Give the position of every malaria parasite and every leukocyte.
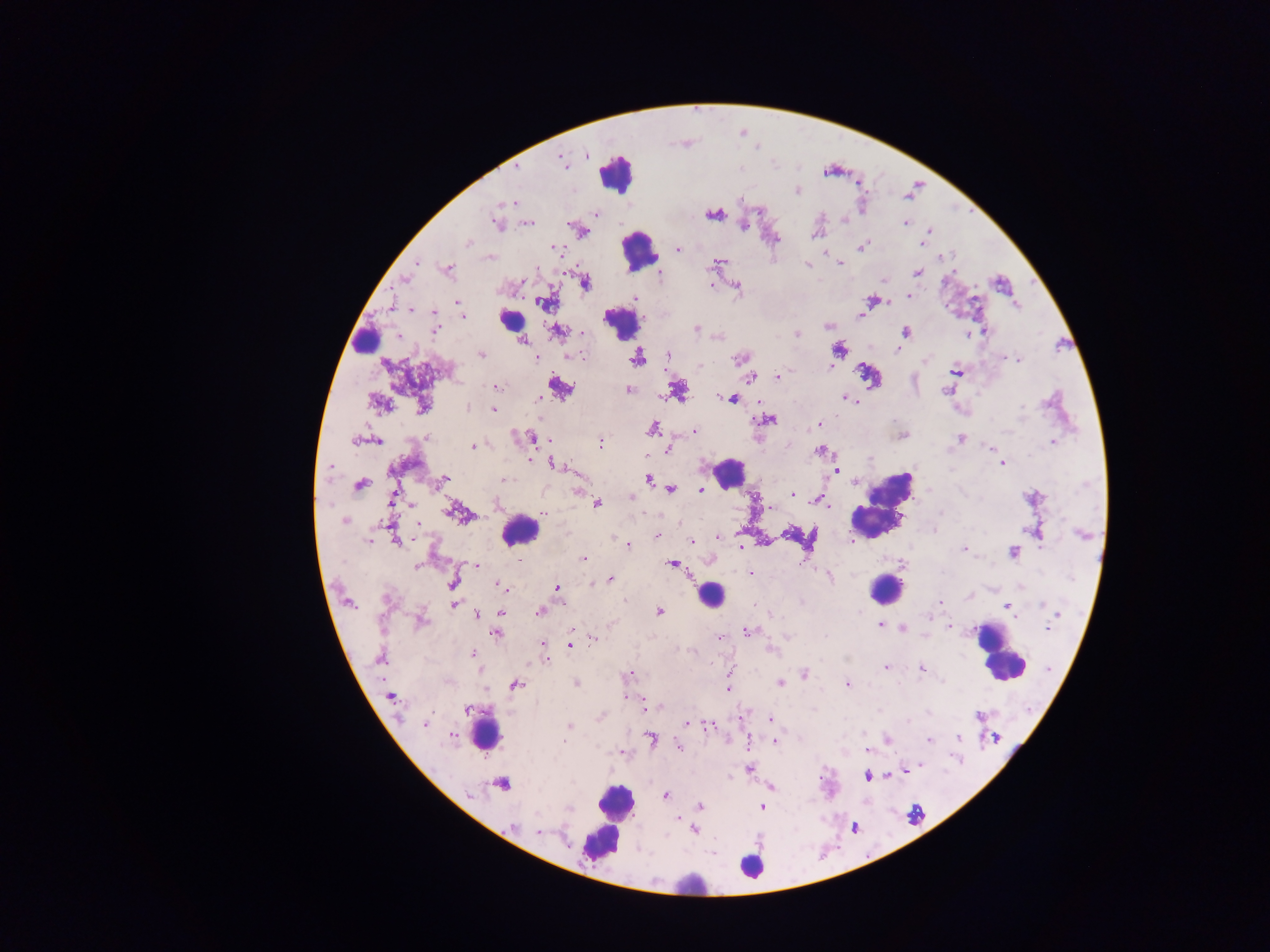
Approximate centers as x y in pixels.
Malaria parasites: 586 154; 561 160; 517 168; 797 190; 508 202; 758 209; 595 213; 713 214; 844 218; 905 222; 496 223; 526 223; 744 225; 582 232; 816 232; 926 236; 468 242; 922 242; 862 246; 555 249; 678 249; 824 251; 490 257; 720 261; 840 263; 416 264; 807 265; 447 270; 917 272; 660 275; 404 280; 584 282; 885 282; 735 284; 710 285; 908 295; 634 298; 871 300; 458 303; 546 303; 1015 304; 409 310; 460 311; 433 313; 861 313; 462 315; 828 327; 694 328; 435 329; 557 330; 906 331; 984 331; 583 332; 796 334; 966 334; 521 338; 898 347; 838 351; 668 354; 480 355; 582 357; 740 357; 636 358; 1003 358; 536 359; 1019 359; 829 366; 956 370; 777 376; 749 377; 558 386; 496 387; 629 389; 677 390; 947 390; 732 398; 846 398; 851 399; 537 400; 378 403; 422 406; 466 407; 493 407; 764 419; 819 425; 651 429; 694 432; 902 434; 426 437; 531 437; 961 439; 362 440; 373 440; 1052 441; 599 443; 472 446; 990 448; 668 449; 820 450; 529 459; 1002 463; 555 464; 329 465; 834 470; 503 479; 648 479; 443 481; 360 484; 702 488; 670 489; 577 491; 630 495; 791 495; 1033 498; 819 499; 392 500; 497 503; 595 503; 456 512; 544 512; 344 520; 1036 530; 716 536; 656 537; 395 538; 369 540; 852 540; 693 542; 629 544; 741 547; 963 550; 1012 551; 518 559; 583 559; 672 564; 415 565; 476 565; 751 573; 830 575; 611 579; 453 585; 501 586; 557 588; 385 599; 940 601; 348 602; 454 604; 1007 606; 539 611; 657 612; 477 613; 501 613; 420 620; 880 625; 950 625; 902 628; 1046 629; 747 632; 496 633; 593 637; 719 637; 570 644; 543 645; 473 654; 380 657; 545 658; 885 668; 920 669; 629 674; 804 675; 576 683; 780 683; 515 684; 847 684; 727 688; 391 696; 623 696; 644 708; 741 717; 770 719; 424 723; 685 724; 568 726; 709 726; 452 735; 958 738; 651 739; 886 739; 774 740; 929 740; 564 741; 747 742; 678 746; 868 750; 621 752; 749 768; 905 771; 867 775; 501 783; 770 787; 665 794; 699 806; 762 807; 677 818; 511 827; 689 827; 694 829; 538 831.
Leukocytes: 615 174; 639 250; 510 319; 621 323; 364 340; 868 377; 728 472; 882 504; 518 530; 886 589; 711 595; 1001 654; 482 730; 615 803; 609 821; 752 866; 689 883.

Summary:
  - Capture: mobile-phone photograph through a microscope
  - Image size: 1270×952 pixels
  - Field of view: single
  - Country: Ghana
  - Preparation: thick blood film